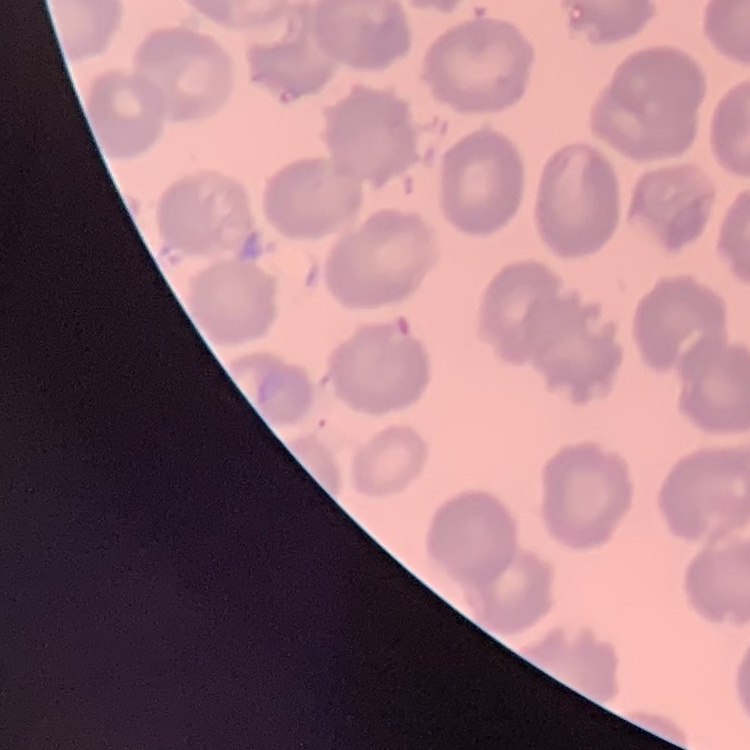

erythrocyte morphology = no rouleaux formation
image type = one tile cut from a larger photomicrograph
preparation = thin blood film
stain = Field's or Giemsa